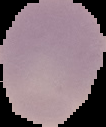

Summary:
  - Image type: segmented cell region on a black background
  - Image size: 106×127 pixels
  - Malaria status: uninfected
  - Preparation: thin blood smear